Classify this cell by malaria status.
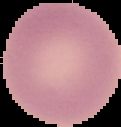
It is uninfected.

image type = segmented cell region with the area outside set to black
preparation = thin blood film
image size = 121×127 pixels